Identify the parasite.
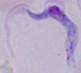
A trypanosome.

1000x magnification. Photomicrograph.